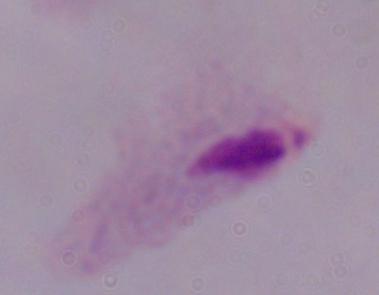

{
  "magnification": "1000x",
  "identification": "trichomonad",
  "modality": "photomicrograph"
}